Give the position of every malaria parasite.
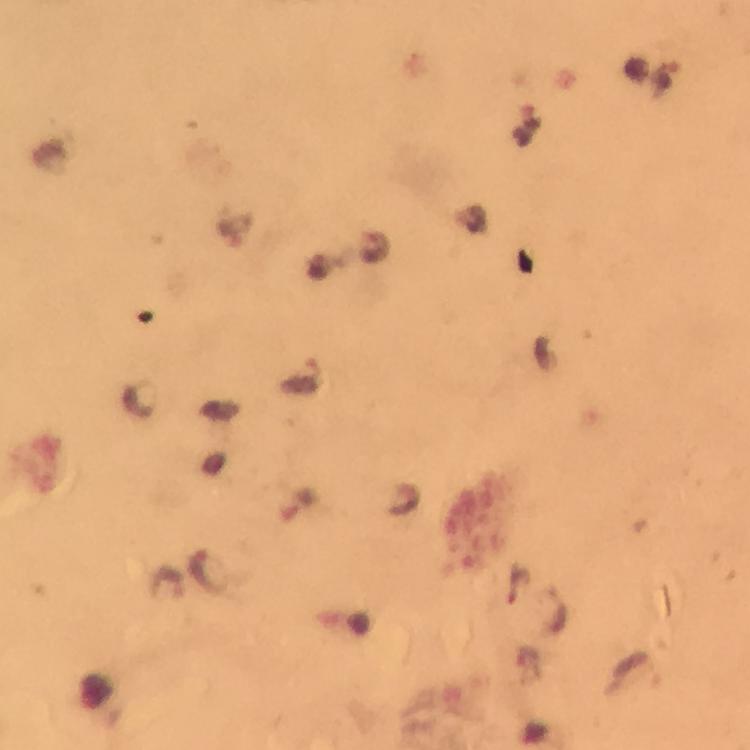
Approximate centers as (x, y) in pixels.
Malaria parasites: (302, 375), (204, 570).

Summary:
  - Capture: smartphone camera through the microscope
  - Magnification: 100x
  - Context: from a diagnostic examination for malaria
  - Immersion oil: used
  - Stain: Giemsa
  - Image size: 750×750 pixels
  - Cropped from: one field of view
  - Preparation: thick blood film